Give the preparation type.
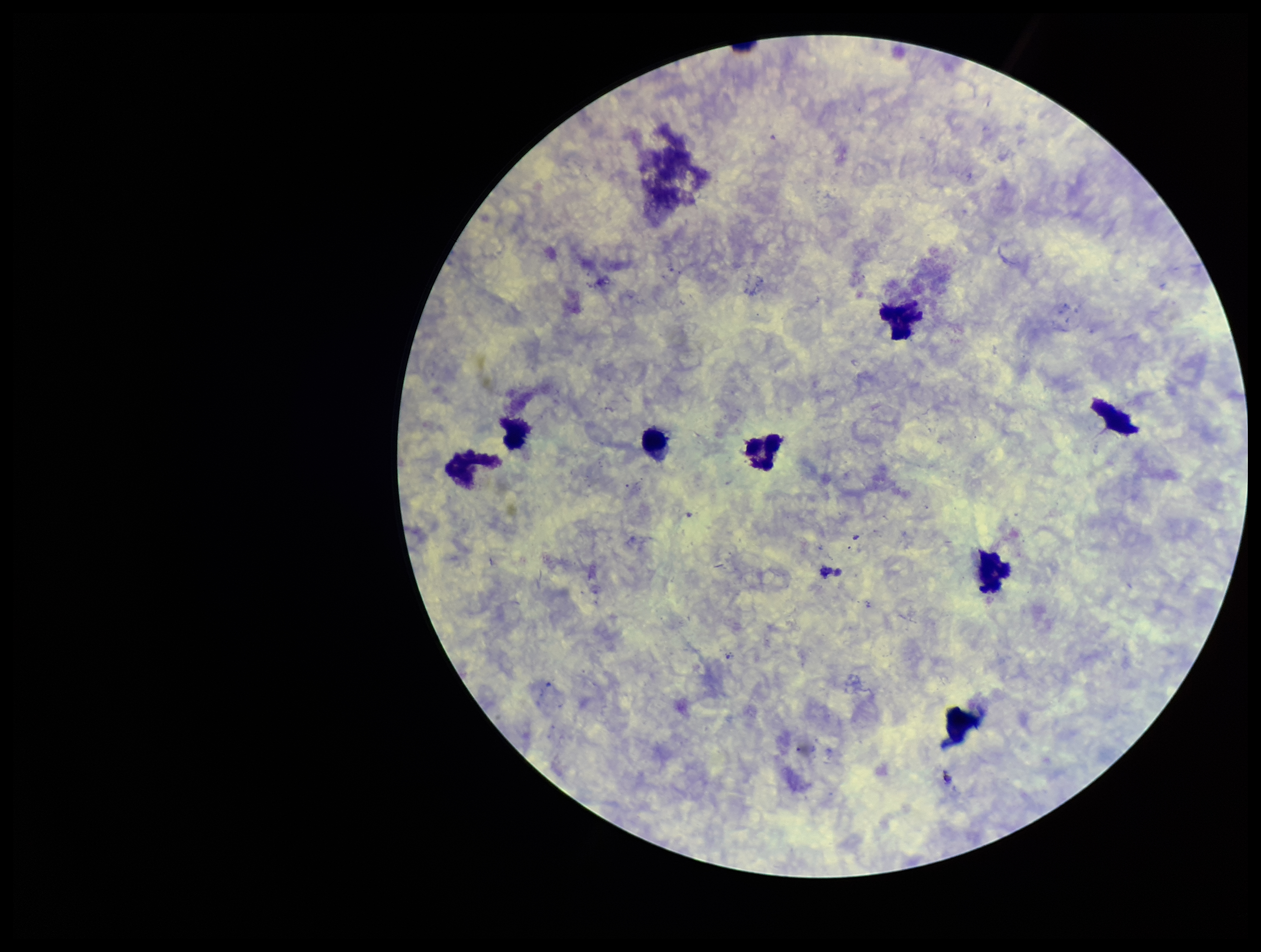
It is a thick blood smear.

Summary:
  - Image size: 1261×952 pixels
  - Patient malaria status: negative
  - Parasite count: 0
  - Capture: smartphone photograph through the microscope eyepiece
  - Plasmodium parasites: none seen
  - Leukocyte count: 8
  - Field of view: one from this slide
  - Stain: Giemsa